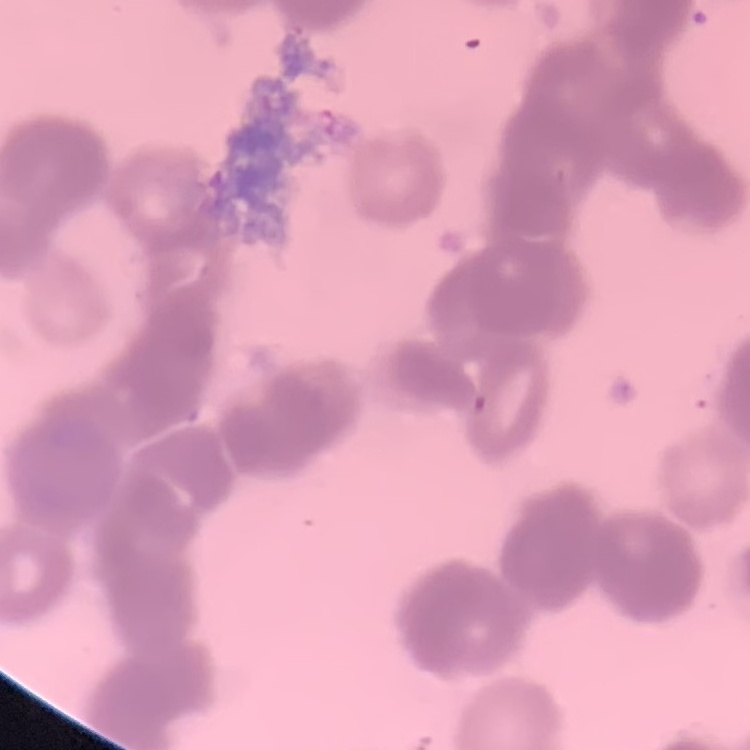
erythrocyte morphology = rouleaux formation
image type = square crop of a larger photomicrograph
stain = Field's or Giemsa
preparation = thin blood smear